Comment on the morphology of the red blood cells.
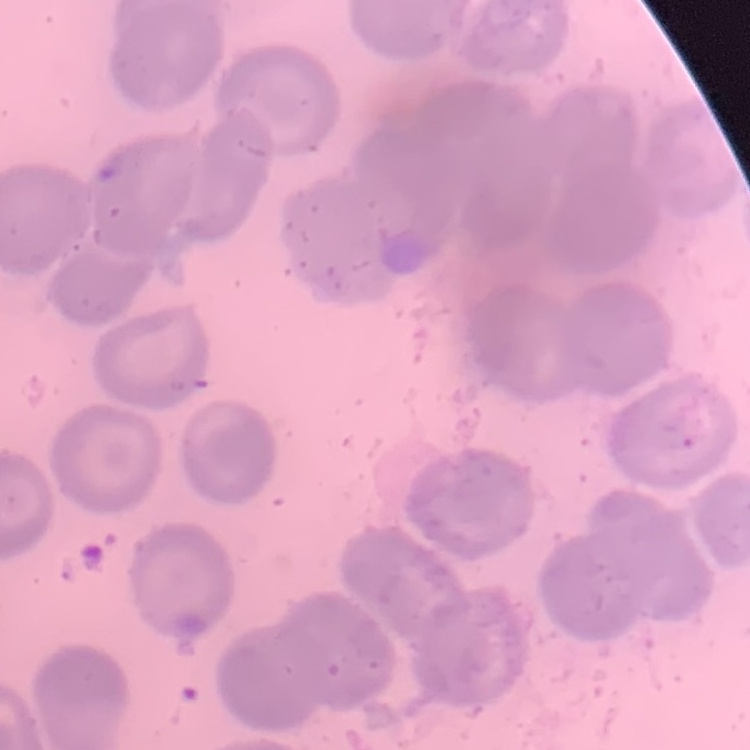
No rouleaux formation.

Summary:
  - Image type: square crop of a larger photomicrograph
  - Preparation: thin blood film
  - Stain: Field's or Giemsa